Outline platelets.
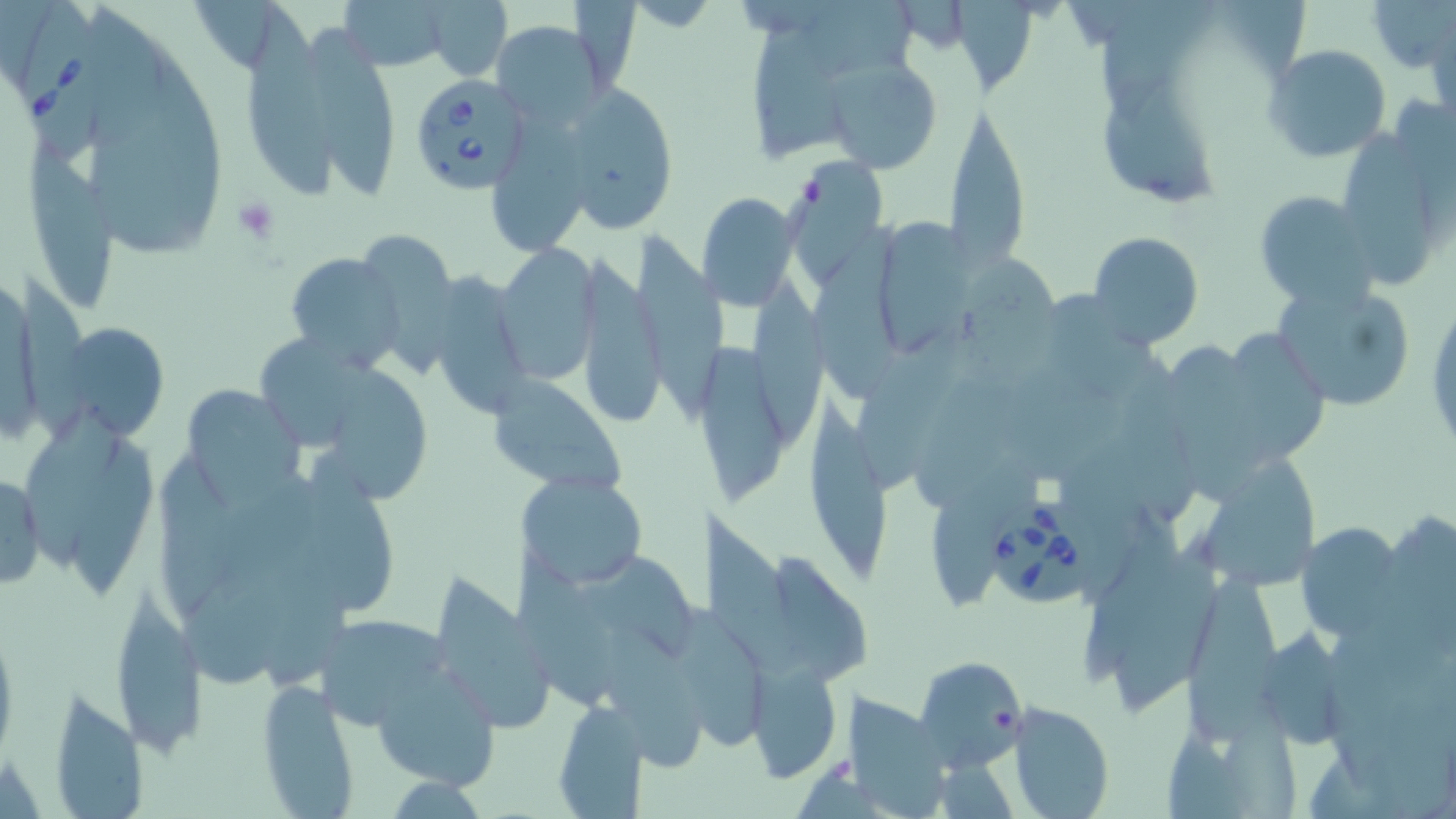
Approximate bounding boxes as (x1, y1, x2, y2) in pixels.
Platelets: (233, 196, 280, 245).

Summary:
  - Babesia divergens-infected red blood cell locations: (15, 0, 110, 164), (407, 70, 535, 196), (987, 489, 1108, 606)
  - Uninfected red blood cell locations: (805, 0, 919, 72), (1223, 0, 1309, 79), (1368, 0, 1455, 71), (334, 1, 456, 72), (425, 1, 512, 81), (952, 1, 1029, 95), (1101, 1, 1217, 128), (248, 2, 334, 197), (88, 4, 165, 150), (754, 17, 843, 172), (488, 20, 613, 130), (313, 23, 394, 200), (1265, 45, 1390, 162), (821, 59, 943, 172), (1101, 81, 1216, 205), (564, 83, 680, 234), (1396, 88, 1456, 242), (944, 97, 1029, 270), (496, 106, 585, 251), (1350, 128, 1435, 289), (29, 141, 117, 308), (792, 158, 891, 294), (1252, 189, 1383, 309), (701, 192, 798, 309), (880, 216, 974, 352), (814, 219, 903, 398), (363, 228, 456, 378), (630, 229, 728, 422), (1087, 232, 1203, 349), (496, 242, 602, 381), (281, 250, 405, 372), (573, 252, 663, 428), (961, 255, 1061, 380), (444, 269, 524, 416), (750, 272, 823, 442), (18, 274, 90, 446), (1270, 279, 1417, 413), (1041, 285, 1164, 398), (1426, 290, 1455, 463), (69, 322, 168, 434), (1231, 325, 1328, 462), (260, 333, 367, 446), (854, 336, 967, 490), (695, 341, 789, 506), (1167, 343, 1264, 502), (326, 365, 436, 503), (916, 368, 1058, 505), (1018, 372, 1125, 480), (485, 377, 630, 495), (188, 378, 307, 511), (806, 388, 898, 591), (25, 404, 124, 569), (73, 429, 156, 595), (929, 449, 1036, 607), (309, 450, 397, 610), (152, 455, 237, 612), (1199, 456, 1319, 587), (0, 472, 47, 594), (517, 472, 648, 590), (215, 482, 343, 581), (700, 507, 797, 674), (1087, 514, 1188, 680), (1300, 520, 1397, 635), (1116, 535, 1228, 711), (516, 550, 613, 705), (588, 552, 701, 658), (779, 556, 873, 680), (261, 563, 354, 689), (437, 571, 551, 729), (1190, 572, 1287, 745), (185, 573, 288, 684), (108, 588, 205, 757), (682, 608, 767, 751), (310, 614, 455, 732), (1262, 624, 1355, 746), (602, 625, 703, 773), (916, 654, 1027, 771), (372, 661, 500, 789), (746, 662, 842, 783), (255, 678, 362, 818), (45, 686, 147, 818), (844, 689, 951, 819), (1225, 694, 1298, 819), (554, 700, 649, 816), (1008, 702, 1115, 819), (1165, 723, 1245, 819)
  - Slide-level diagnosis: Babesia divergens
  - Stain: May-Grünwald-Giemsa
  - Preparation: thin blood film
  - Image size: 1456×819 pixels
  - Modality: optical microscopy
  - Magnification: 1000x
  - Field of view: single